Give the position of every malaria parasite.
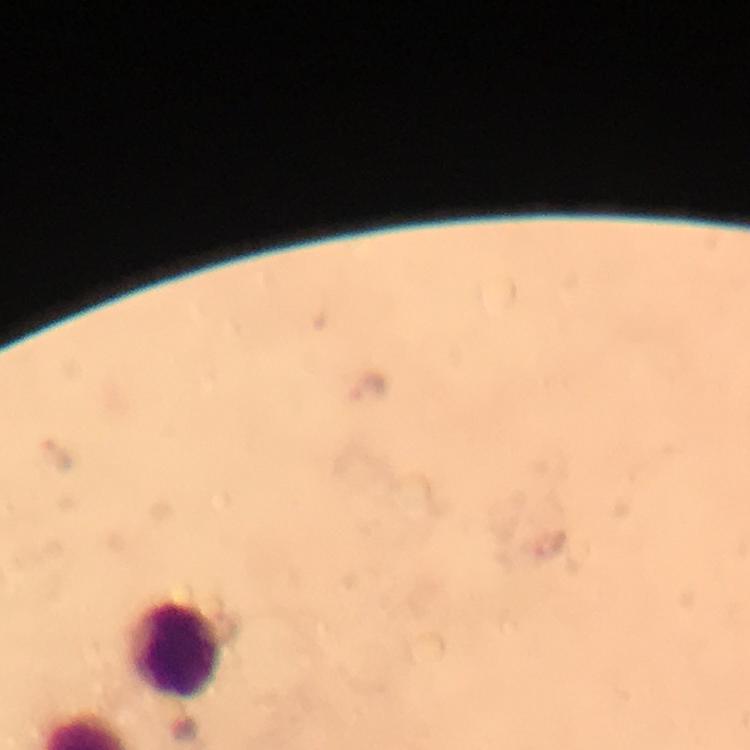
Approximate object centers, in pixels from the top-left corner.
Malaria parasites: (x=366, y=385), (x=61, y=458).

{
  "capture": "smartphone mounted on the microscope",
  "preparation": "thick blood smear",
  "image_size": "750×750 pixels",
  "magnification": "100x",
  "cropped_from": "a single field of view",
  "leukocyte_locations": "approximate object centers, in pixels from the top-left corner: (x=176, y=647)",
  "context": "from a malaria diagnostic workup",
  "immersion_oil": "used",
  "stain": "Giemsa"
}